Report the malaria status of this cell.
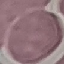

It is uninfected.

Automatically extracted cell patch, resized to 64 × 64 pixels. Photographed with a smartphone camera at the microscope eyepiece. Thin smear of blood. Giemsa-stained preparation.